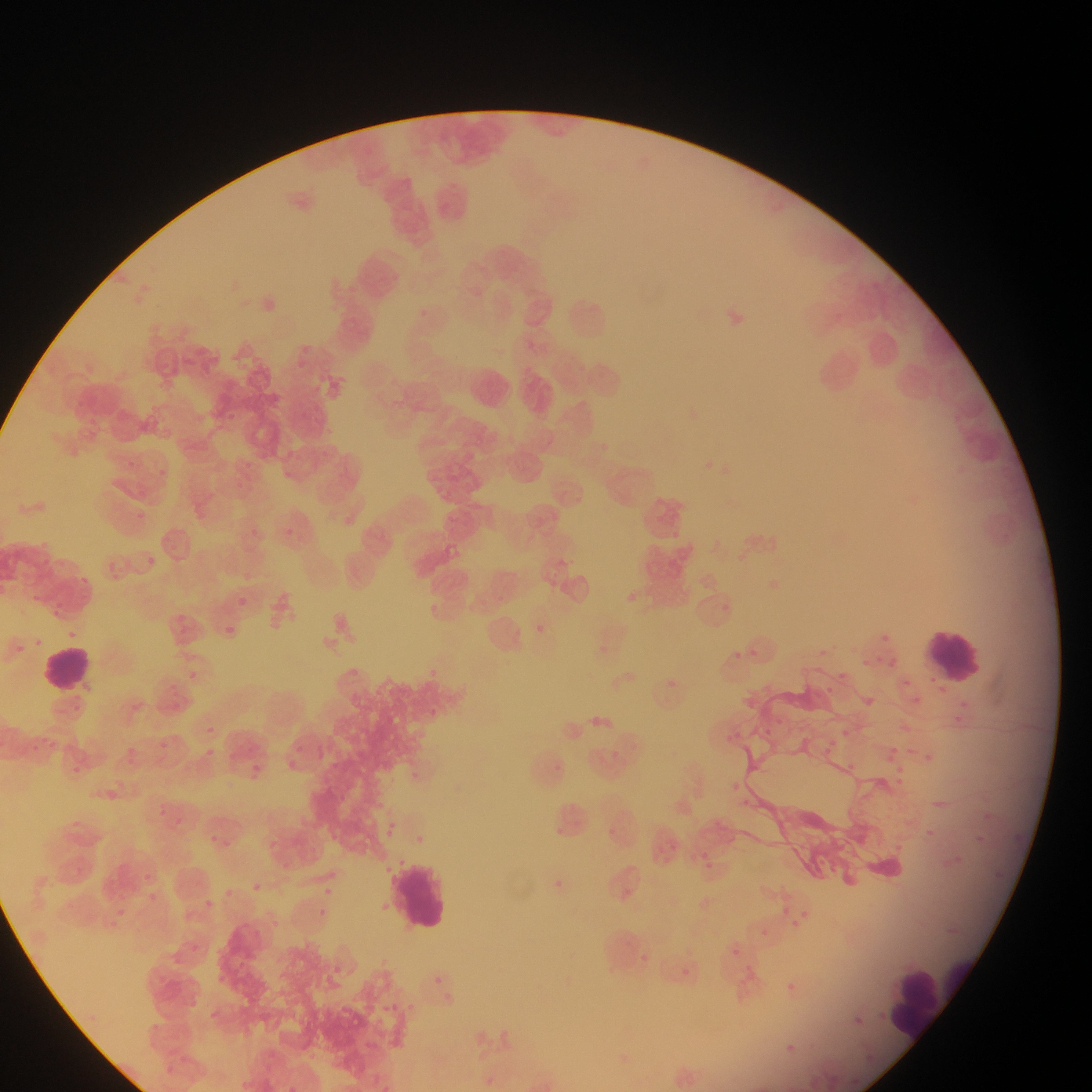
Approximate bounding boxes as (left, top, right, bottom) in pixels.
Summary:
  - Malaria parasite locations: (704, 456, 727, 475), (156, 464, 174, 484), (135, 484, 148, 504), (131, 508, 144, 524), (245, 523, 262, 543), (673, 524, 687, 537), (143, 557, 158, 570), (108, 558, 121, 580), (78, 573, 88, 589), (627, 586, 644, 605), (33, 594, 40, 606), (238, 594, 251, 608), (51, 600, 69, 618), (533, 620, 549, 637), (222, 621, 232, 634), (877, 626, 895, 648), (65, 627, 76, 642), (816, 642, 832, 658), (749, 643, 762, 656), (732, 646, 739, 658), (859, 652, 871, 665), (877, 652, 885, 665), (892, 653, 902, 669), (181, 667, 202, 686), (833, 667, 851, 684), (905, 677, 915, 692), (821, 682, 837, 698), (869, 694, 879, 705), (913, 696, 924, 708), (960, 700, 967, 708), (423, 707, 442, 717), (585, 710, 616, 738), (949, 710, 968, 731), (781, 711, 794, 724), (204, 719, 223, 735), (902, 720, 910, 738), (842, 721, 852, 740), (762, 723, 775, 737), (730, 724, 743, 742), (172, 728, 191, 748), (292, 734, 309, 753), (153, 738, 169, 755), (198, 742, 222, 765), (887, 743, 902, 759), (122, 744, 141, 768), (919, 750, 937, 767), (289, 752, 305, 777), (884, 753, 896, 766), (845, 756, 855, 773), (243, 759, 267, 783), (896, 764, 906, 776), (410, 766, 419, 785), (102, 776, 121, 806), (891, 776, 902, 789), (726, 778, 742, 798), (738, 794, 753, 818), (163, 805, 173, 819), (983, 809, 996, 821), (383, 819, 399, 842), (604, 822, 617, 834), (206, 825, 224, 851), (924, 825, 936, 840), (1012, 830, 1024, 843), (417, 831, 428, 845), (661, 840, 670, 857), (222, 844, 236, 859), (950, 851, 966, 866), (697, 855, 718, 875), (815, 858, 837, 880), (75, 859, 94, 878), (141, 866, 155, 886), (989, 868, 1005, 881), (540, 872, 572, 900), (248, 880, 264, 895), (220, 884, 236, 901), (318, 884, 335, 900), (143, 891, 165, 904), (203, 894, 222, 917), (114, 903, 133, 917), (779, 903, 792, 917), (314, 905, 330, 920), (790, 908, 814, 929), (97, 909, 123, 930), (757, 926, 771, 939), (190, 940, 208, 961), (726, 945, 741, 959), (637, 953, 650, 966), (678, 962, 688, 977), (151, 968, 171, 991), (434, 970, 450, 989), (212, 971, 237, 990), (781, 979, 798, 995), (185, 997, 202, 1013), (405, 998, 416, 1014), (387, 999, 400, 1015), (850, 1012, 864, 1031), (778, 1038, 801, 1058), (863, 1054, 872, 1065), (164, 1062, 180, 1084), (289, 1084, 304, 1092) | approximate (x, y) pixel centers of objects too small to bound: (128, 460), (829, 742), (979, 835)
  - Leukocyte locations: (429, 178, 479, 231), (395, 189, 470, 243), (391, 203, 435, 241), (559, 290, 617, 347), (465, 364, 516, 411), (924, 623, 990, 690), (38, 644, 95, 694), (387, 860, 455, 933), (888, 963, 948, 1037)
  - Country: Ghana
  - Preparation: thin blood film
  - Capture: mobile-phone photograph through a microscope
  - Image size: 1092×1092 pixels
  - Field of view: single